Assess this cell for malaria.
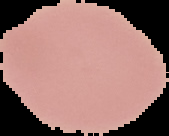
Uninfected.

Summary:
  - Preparation: thin blood smear
  - Image size: 169×136 pixels
  - Image type: segmented cell region with the area outside set to black